Assess this cell for malaria.
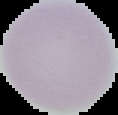

Uninfected.

image type = segmented cell region on a black background
image size = 118×115 pixels
preparation = thin blood smear